Outline platelets.
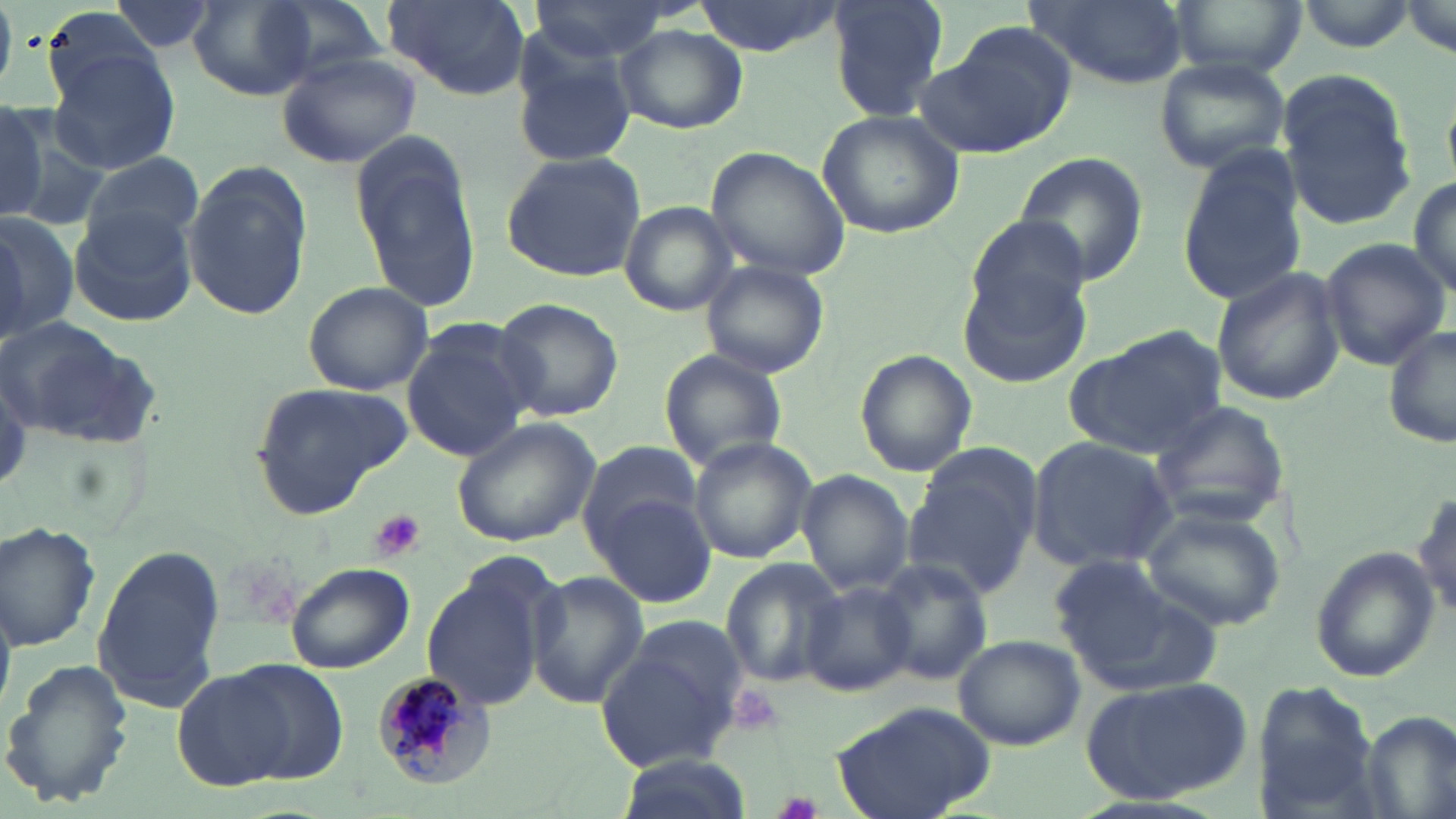

Approximate bounding boxes as [x1, y1, x2, y2] in pixels.
Platelets: [366, 509, 427, 563], [726, 683, 783, 737], [776, 791, 823, 819].

slide-level diagnosis = Plasmodium malariae
magnification = 1000x
stain = May-Grünwald-Giemsa
field of view = single
uninfected red blood cell locations = approximate bounding boxes as [x1, y1, x2, y2] in pixels: [256, 0, 389, 84], [381, 0, 531, 102], [690, 0, 850, 57], [825, 0, 952, 122], [1025, 0, 1190, 90], [1167, 0, 1308, 78], [1297, 0, 1419, 51], [526, 1, 667, 64], [185, 2, 321, 98], [38, 7, 172, 112], [615, 24, 747, 135], [916, 24, 1077, 159], [509, 35, 635, 168], [46, 48, 183, 175], [277, 49, 424, 168], [1155, 59, 1292, 174], [1274, 70, 1421, 230], [0, 100, 50, 226], [815, 110, 965, 241], [352, 135, 480, 307], [704, 144, 850, 283], [1176, 148, 1310, 308], [500, 151, 649, 282], [80, 152, 205, 255], [1013, 152, 1148, 285], [182, 163, 311, 321], [1408, 176, 1456, 299], [620, 202, 739, 314], [69, 208, 196, 329], [0, 214, 80, 341], [965, 215, 1093, 331], [1318, 238, 1450, 365], [698, 259, 830, 379], [1210, 266, 1349, 405], [958, 268, 1093, 388], [301, 281, 433, 395], [492, 297, 624, 425], [1, 315, 158, 444], [1383, 322, 1456, 452], [401, 323, 536, 460], [1064, 327, 1230, 459], [660, 348, 788, 470], [854, 349, 977, 475], [250, 378, 410, 512], [1151, 399, 1291, 529], [451, 417, 601, 547], [1026, 437, 1178, 572], [687, 438, 815, 564], [577, 441, 704, 550], [904, 445, 1044, 597], [797, 469, 915, 596], [887, 478, 1024, 671], [1412, 484, 1454, 625], [589, 493, 717, 607], [1140, 505, 1285, 631], [1, 522, 102, 649], [90, 543, 223, 714], [1310, 546, 1440, 683], [1044, 554, 1204, 692], [719, 559, 843, 689], [870, 559, 993, 688], [286, 562, 414, 675], [420, 570, 550, 710], [526, 571, 649, 709], [802, 580, 915, 696], [596, 616, 752, 772], [953, 633, 1086, 750], [2, 660, 134, 809], [216, 660, 350, 788], [170, 669, 300, 793], [1080, 679, 1256, 804], [1254, 681, 1382, 811], [828, 701, 998, 819], [1358, 709, 1455, 817], [615, 755, 743, 819]
modality = optical microscopy
image size = 1456×819 pixels
preparation = thin blood smear
Plasmodium malariae-infected red blood cell locations = approximate bounding boxes as [x1, y1, x2, y2] in pixels: [374, 672, 496, 791]